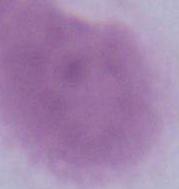
identification = red blood cell
modality = micrograph
magnification = 1000x